Outline each Plasmodium falciparum-infected red blood cell.
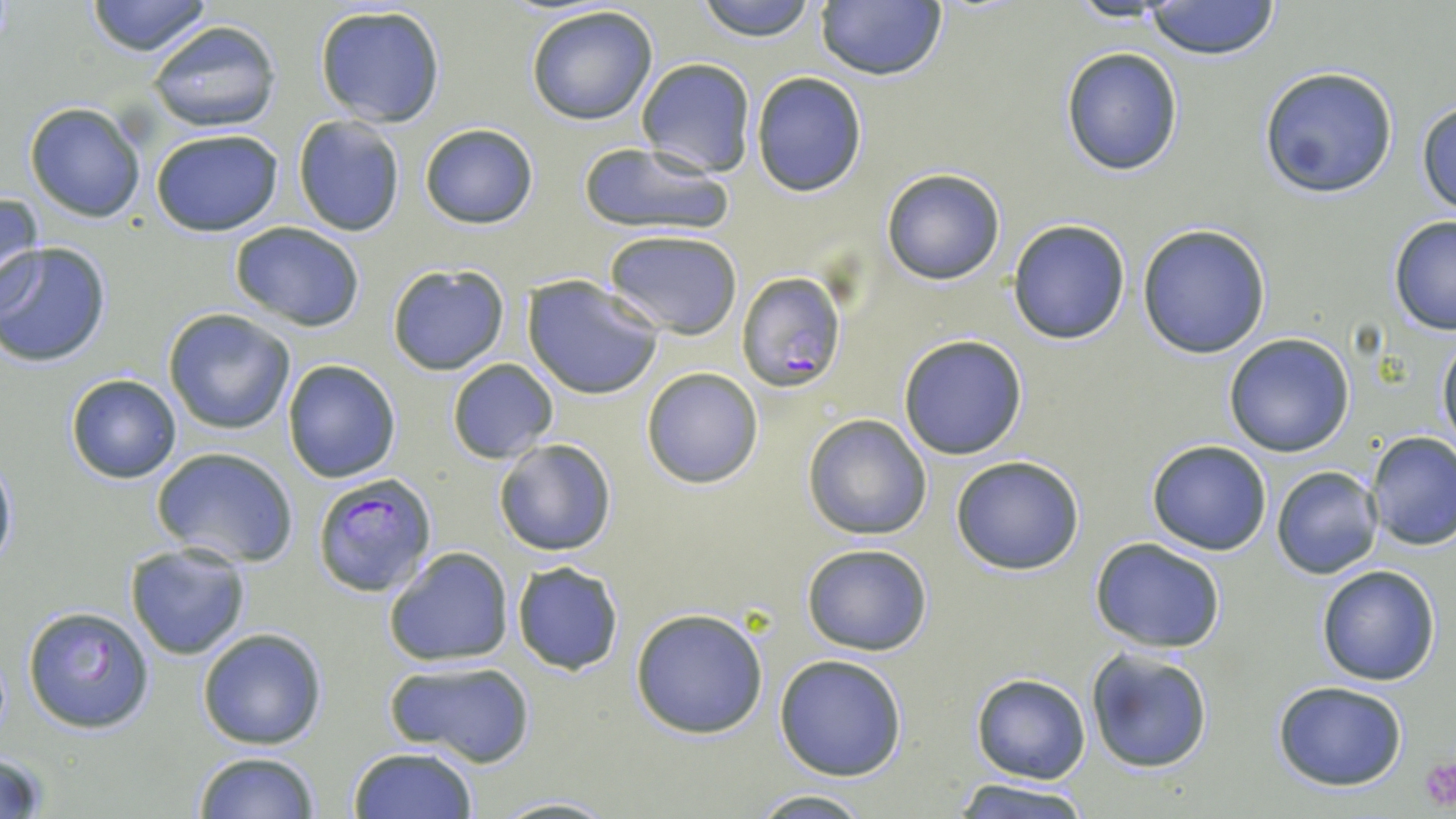

Approximate bounding boxes as named x1/y1/x2/y2 corners in pixels.
Plasmodium falciparum-infected red blood cells: (x1=736, y1=271, x2=845, y2=392), (x1=311, y1=472, x2=438, y2=601).

Summary:
  - Uninfected red blood cell locations: (x1=83, y1=0, x2=214, y2=56), (x1=693, y1=0, x2=822, y2=43), (x1=813, y1=1, x2=947, y2=82), (x1=1142, y1=1, x2=1282, y2=62), (x1=314, y1=4, x2=447, y2=127), (x1=524, y1=6, x2=662, y2=126), (x1=146, y1=20, x2=282, y2=133), (x1=1059, y1=46, x2=1184, y2=177), (x1=634, y1=57, x2=757, y2=177), (x1=1257, y1=65, x2=1399, y2=199), (x1=749, y1=72, x2=868, y2=196), (x1=1416, y1=100, x2=1456, y2=218), (x1=24, y1=101, x2=146, y2=222), (x1=292, y1=115, x2=406, y2=237), (x1=419, y1=124, x2=539, y2=228), (x1=150, y1=128, x2=285, y2=238), (x1=578, y1=141, x2=733, y2=235), (x1=880, y1=168, x2=1007, y2=286), (x1=0, y1=192, x2=45, y2=309), (x1=1388, y1=215, x2=1456, y2=337), (x1=1007, y1=219, x2=1131, y2=344), (x1=229, y1=222, x2=367, y2=332), (x1=1136, y1=223, x2=1272, y2=360), (x1=605, y1=229, x2=743, y2=338), (x1=0, y1=240, x2=111, y2=367), (x1=386, y1=264, x2=509, y2=374), (x1=522, y1=277, x2=665, y2=399), (x1=162, y1=309, x2=296, y2=435), (x1=1436, y1=331, x2=1456, y2=453), (x1=1223, y1=333, x2=1355, y2=457), (x1=898, y1=334, x2=1029, y2=460), (x1=281, y1=358, x2=402, y2=482), (x1=446, y1=358, x2=559, y2=464), (x1=640, y1=367, x2=763, y2=488), (x1=65, y1=373, x2=182, y2=483), (x1=802, y1=414, x2=932, y2=540), (x1=1366, y1=431, x2=1456, y2=550), (x1=492, y1=438, x2=618, y2=556), (x1=1146, y1=440, x2=1272, y2=555), (x1=152, y1=447, x2=299, y2=568), (x1=0, y1=451, x2=17, y2=573), (x1=950, y1=456, x2=1085, y2=574), (x1=1272, y1=465, x2=1382, y2=578), (x1=1089, y1=537, x2=1227, y2=654), (x1=124, y1=542, x2=253, y2=661), (x1=801, y1=542, x2=934, y2=657), (x1=383, y1=546, x2=515, y2=668), (x1=510, y1=562, x2=626, y2=675), (x1=1315, y1=565, x2=1441, y2=685), (x1=21, y1=604, x2=155, y2=735), (x1=630, y1=606, x2=769, y2=740), (x1=196, y1=627, x2=327, y2=750), (x1=1085, y1=649, x2=1214, y2=773), (x1=774, y1=654, x2=908, y2=781), (x1=384, y1=657, x2=537, y2=764), (x1=970, y1=674, x2=1089, y2=784), (x1=1271, y1=680, x2=1409, y2=790), (x1=348, y1=745, x2=479, y2=818), (x1=192, y1=751, x2=321, y2=819), (x1=0, y1=752, x2=51, y2=819), (x1=949, y1=778, x2=1096, y2=818), (x1=744, y1=791, x2=881, y2=818), (x1=487, y1=795, x2=621, y2=818)
  - Platelet locations: (x1=1418, y1=755, x2=1456, y2=812)
  - Slide-level diagnosis: Plasmodium falciparum
  - Magnification: 1000x
  - Modality: light microscopy
  - Image size: 1456×819 pixels
  - Stain: May-Grünwald-Giemsa
  - Preparation: thin blood smear
  - Field of view: one of a larger specimen